Name the cell type shown.
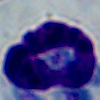

This is a leukocyte.

1000x magnification. Photomicrograph.